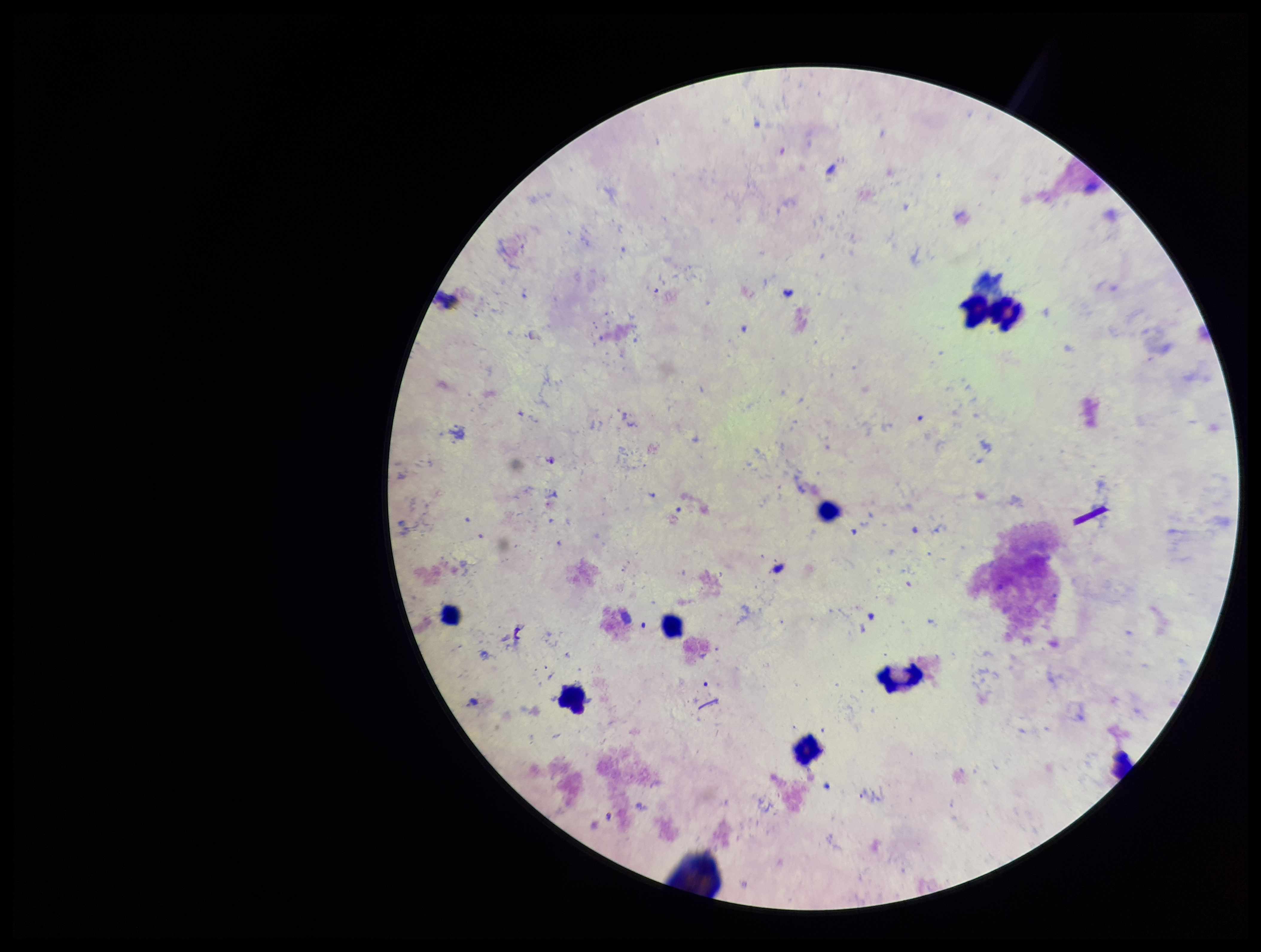 Photographed through the microscope eyepiece with a smartphone camera. Stained with Giemsa. Image is 1261×952 pixels. One field from this slide. Plasmodium parasites: none detected. Preparation: thick smear. Leukocyte count: 8. Parasite count: 0. Patient malaria status: negative.